Give the extent of all Plasmodium falciparum-infected red blood cells.
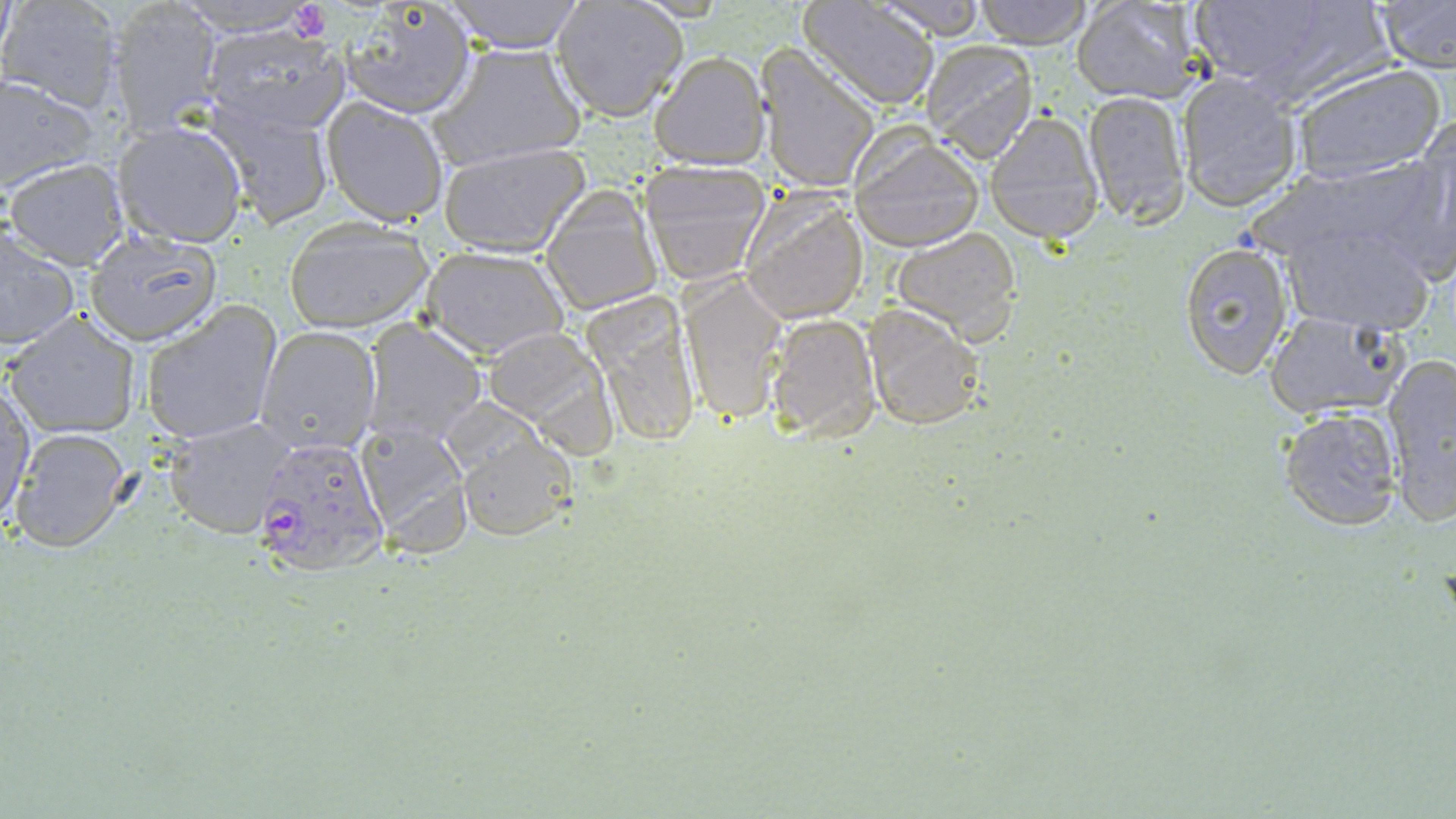
Approximate bounding boxes as (x1,y1)-(x2,y2) corner pairs in pixels.
Plasmodium falciparum-infected red blood cells: (252,434)-(389,577).

slide-level diagnosis = Plasmodium falciparum
magnification = 1000x
uninfected red blood cell locations = approximate bounding boxes as (x1,y1)-(x2,y2) corner pairs in pixels: (0,0)-(125,114), (169,0)-(325,35), (442,0)-(586,53), (798,0)-(940,110), (869,0)-(989,40), (974,0)-(1092,48), (1071,0)-(1209,105), (1183,0)-(1387,98), (1370,1)-(1456,74), (109,2)-(222,135), (551,2)-(687,122), (337,3)-(478,120), (200,24)-(351,137), (920,40)-(1041,163), (435,42)-(588,169), (756,45)-(881,193), (650,51)-(768,169), (1287,62)-(1449,185), (1176,70)-(1303,213), (0,73)-(99,194), (1081,90)-(1190,226), (205,95)-(335,229), (322,97)-(449,226), (983,111)-(1105,244), (113,118)-(248,247), (1394,120)-(1456,280), (850,132)-(984,252), (439,141)-(593,258), (1261,154)-(1448,279), (4,158)-(130,269), (637,158)-(773,284), (540,184)-(662,316), (739,190)-(870,323), (1278,217)-(1436,336), (283,219)-(434,333), (1,224)-(80,354), (889,227)-(1024,341), (84,232)-(221,346), (1177,241)-(1294,380), (421,246)-(569,359), (678,271)-(789,424), (583,292)-(701,451), (140,301)-(283,446), (861,304)-(986,430), (1262,310)-(1405,420), (7,313)-(140,438), (765,314)-(882,445), (362,321)-(485,444), (255,327)-(380,457), (483,327)-(619,454), (1383,353)-(1456,522), (1,378)-(36,528), (1278,406)-(1403,532), (163,417)-(298,538), (353,417)-(473,556), (9,428)-(133,553), (455,433)-(576,542)
image size = 1456×819 pixels
field of view = single
stain = May-Grünwald-Giemsa
preparation = thin blood smear
platelet locations = approximate bounding boxes as (x1,y1)-(x2,y2) corner pairs in pixels: (289,2)-(330,43)
modality = light microscopy